Report the malaria status of this cell.
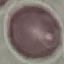
It is uninfected.

Giemsa stain. Thin blood film. Automatically extracted cell patch, resized to 64 × 64 pixels. Photographed with a smartphone camera at the microscope eyepiece.